Describe the morphology of the erythrocytes.
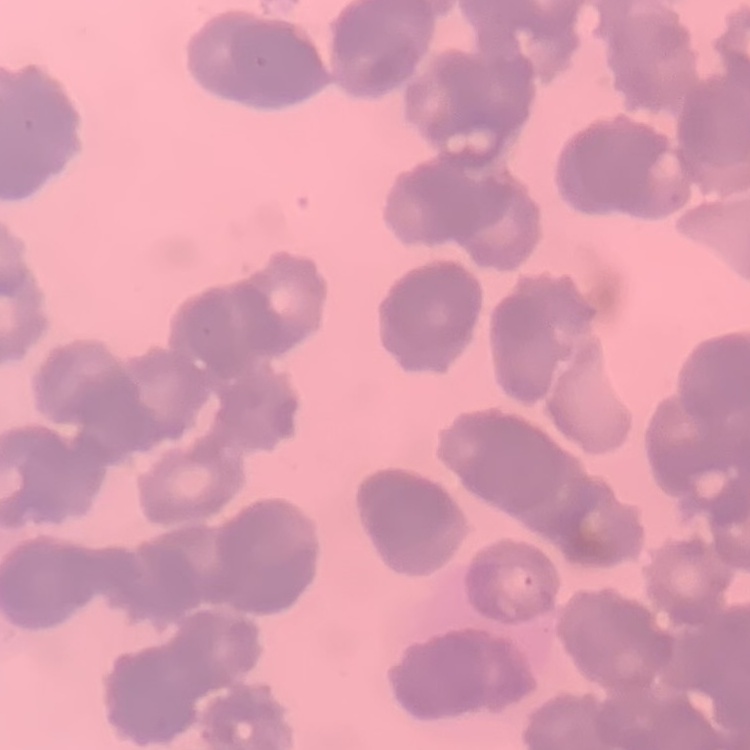
Rouleaux formation.

Thin blood film. One tile cut from a larger photomicrograph. Field's or Giemsa stain.